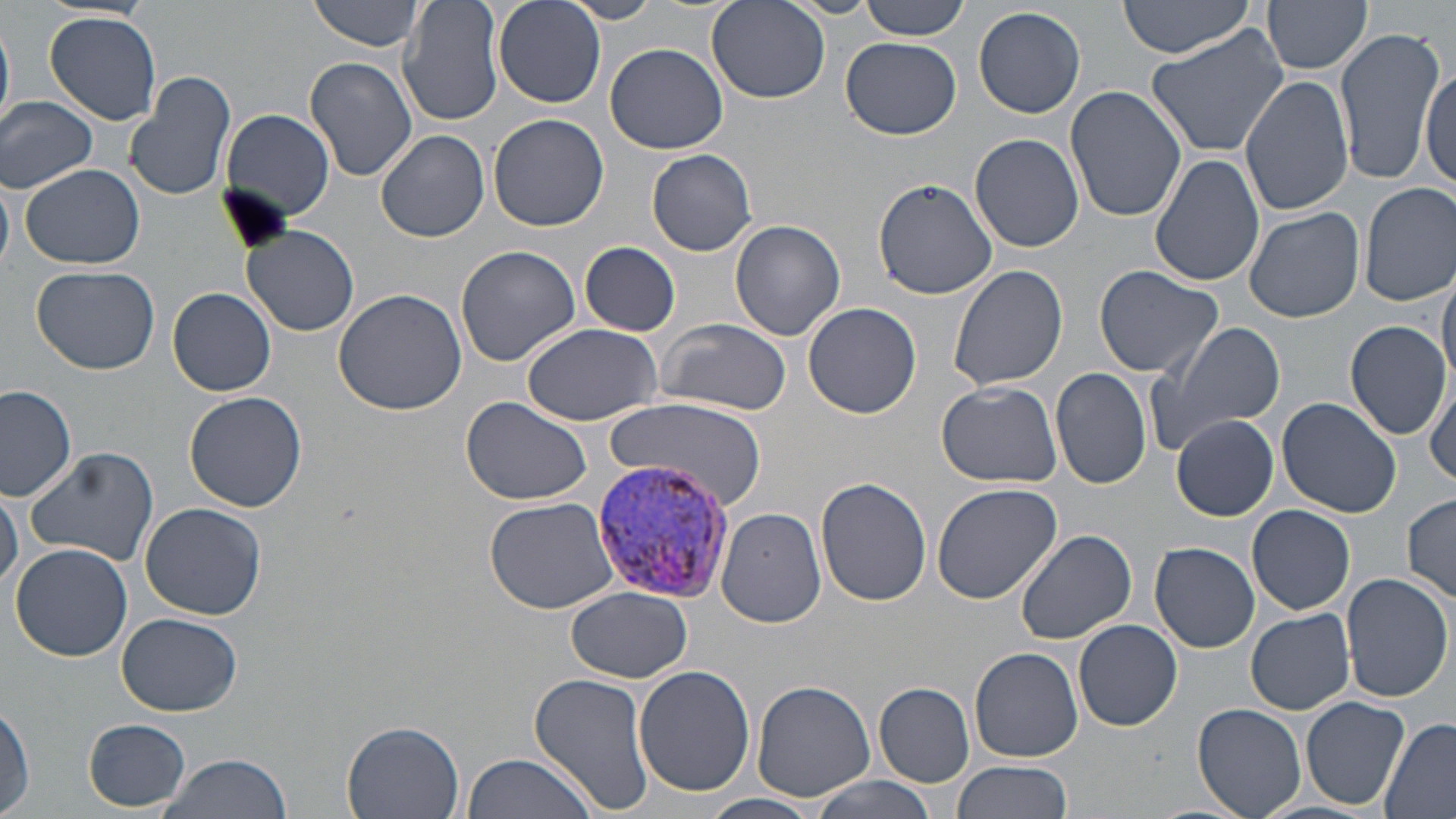

{
  "plasmodium_vivax_infected_red_blood_cell_locations": "approximate bounding boxes as named x1/y1/x2/y2 corners in pixels: (x1=586, y1=458, x2=737, y2=608)",
  "slide_level_diagnosis": "Plasmodium vivax",
  "preparation": "thin blood film",
  "magnification": "1000x",
  "platelet_locations": "approximate bounding boxes as named x1/y1/x2/y2 corners in pixels: (x1=216, y1=183, x2=294, y2=255)",
  "modality": "light microscopy",
  "stain": "May-Grünwald-Giemsa",
  "field_of_view": "single",
  "uninfected_red_blood_cell_locations": "approximate bounding boxes as named x1/y1/x2/y2 corners in pixels: (x1=307, y1=0, x2=429, y2=52), (x1=397, y1=0, x2=504, y2=126), (x1=494, y1=0, x2=606, y2=109), (x1=563, y1=0, x2=663, y2=23), (x1=858, y1=0, x2=972, y2=40), (x1=1118, y1=0, x2=1253, y2=58), (x1=1266, y1=0, x2=1372, y2=76), (x1=707, y1=2, x2=831, y2=104), (x1=972, y1=6, x2=1086, y2=119), (x1=45, y1=12, x2=162, y2=126), (x1=0, y1=14, x2=14, y2=135), (x1=1147, y1=24, x2=1291, y2=157), (x1=1332, y1=25, x2=1443, y2=187), (x1=842, y1=36, x2=961, y2=140), (x1=604, y1=42, x2=729, y2=154), (x1=304, y1=55, x2=417, y2=183), (x1=1420, y1=60, x2=1453, y2=196), (x1=125, y1=69, x2=238, y2=203), (x1=1239, y1=75, x2=1354, y2=215), (x1=1066, y1=88, x2=1187, y2=224), (x1=0, y1=96, x2=98, y2=194), (x1=222, y1=110, x2=336, y2=221), (x1=488, y1=114, x2=609, y2=232), (x1=376, y1=129, x2=489, y2=243), (x1=971, y1=133, x2=1084, y2=253), (x1=646, y1=148, x2=757, y2=254), (x1=1150, y1=151, x2=1265, y2=287), (x1=19, y1=164, x2=144, y2=270), (x1=0, y1=174, x2=15, y2=270), (x1=875, y1=179, x2=995, y2=299), (x1=1357, y1=182, x2=1456, y2=307), (x1=1243, y1=206, x2=1365, y2=322), (x1=730, y1=220, x2=844, y2=342), (x1=241, y1=225, x2=361, y2=337), (x1=579, y1=242, x2=681, y2=335), (x1=454, y1=245, x2=581, y2=367), (x1=948, y1=264, x2=1068, y2=392), (x1=31, y1=265, x2=162, y2=374), (x1=1437, y1=265, x2=1456, y2=385), (x1=1093, y1=267, x2=1223, y2=378), (x1=168, y1=287, x2=278, y2=397), (x1=333, y1=287, x2=466, y2=416), (x1=803, y1=303, x2=919, y2=419), (x1=654, y1=317, x2=793, y2=417), (x1=1145, y1=319, x2=1285, y2=455), (x1=1346, y1=319, x2=1449, y2=440), (x1=518, y1=322, x2=666, y2=426), (x1=1049, y1=369, x2=1153, y2=492), (x1=1427, y1=371, x2=1456, y2=489), (x1=934, y1=381, x2=1061, y2=489), (x1=0, y1=385, x2=78, y2=500), (x1=185, y1=391, x2=308, y2=513), (x1=461, y1=396, x2=591, y2=506), (x1=1278, y1=396, x2=1401, y2=518), (x1=605, y1=400, x2=767, y2=505), (x1=1171, y1=414, x2=1279, y2=520), (x1=24, y1=446, x2=159, y2=565), (x1=816, y1=477, x2=933, y2=608), (x1=930, y1=483, x2=1062, y2=607), (x1=0, y1=486, x2=22, y2=593), (x1=1402, y1=493, x2=1456, y2=605), (x1=483, y1=495, x2=622, y2=614), (x1=140, y1=502, x2=267, y2=620), (x1=1248, y1=505, x2=1356, y2=615), (x1=717, y1=507, x2=827, y2=629), (x1=1017, y1=530, x2=1137, y2=645), (x1=10, y1=542, x2=133, y2=663), (x1=1149, y1=542, x2=1261, y2=653), (x1=1341, y1=572, x2=1451, y2=702), (x1=566, y1=587, x2=692, y2=682), (x1=1244, y1=609, x2=1356, y2=715), (x1=115, y1=612, x2=244, y2=716), (x1=1073, y1=619, x2=1183, y2=731), (x1=971, y1=648, x2=1082, y2=762), (x1=634, y1=666, x2=756, y2=796), (x1=529, y1=672, x2=656, y2=816), (x1=753, y1=682, x2=876, y2=800), (x1=873, y1=683, x2=974, y2=786), (x1=1301, y1=695, x2=1410, y2=810), (x1=1194, y1=702, x2=1307, y2=819), (x1=0, y1=703, x2=34, y2=818), (x1=1377, y1=717, x2=1455, y2=817), (x1=83, y1=718, x2=191, y2=810), (x1=341, y1=722, x2=464, y2=818), (x1=461, y1=753, x2=597, y2=819), (x1=152, y1=754, x2=294, y2=819), (x1=952, y1=759, x2=1074, y2=819), (x1=801, y1=774, x2=940, y2=819), (x1=698, y1=793, x2=827, y2=819), (x1=1255, y1=800, x2=1383, y2=819)",
  "image_size": "1456×819 pixels"
}